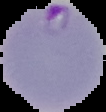

The area outside the segmented cell region is set to black. Image is 106×112 pixels. Malaria status: parasitized. From a thin blood film.